Assess this cell for malaria.
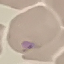
It is uninfected.

Thin blood smear. Acquired by smartphone through the microscope eyepiece. Giemsa-stained preparation. Automatically extracted cell patch, resized to 64 × 64 pixels.